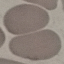

Summary:
  - Result: no malaria parasites seen
  - Preparation: thin blood film
  - Image type: cell patch, automatically extracted from a larger field of view and resized to 64 × 64 pixels
  - Stain: Giemsa
  - Capture: smartphone through the microscope eyepiece